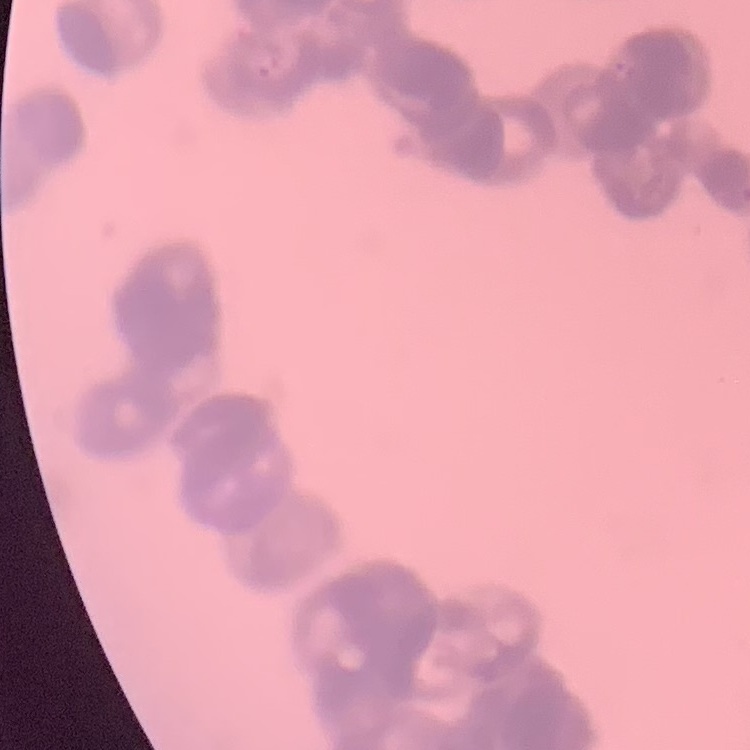
Summary:
  - Erythrocyte morphology: rouleaux formation
  - Preparation: thin blood smear
  - Stain: Field's or Giemsa
  - Image type: square crop of a larger photomicrograph